Describe the morphology of the erythrocytes.
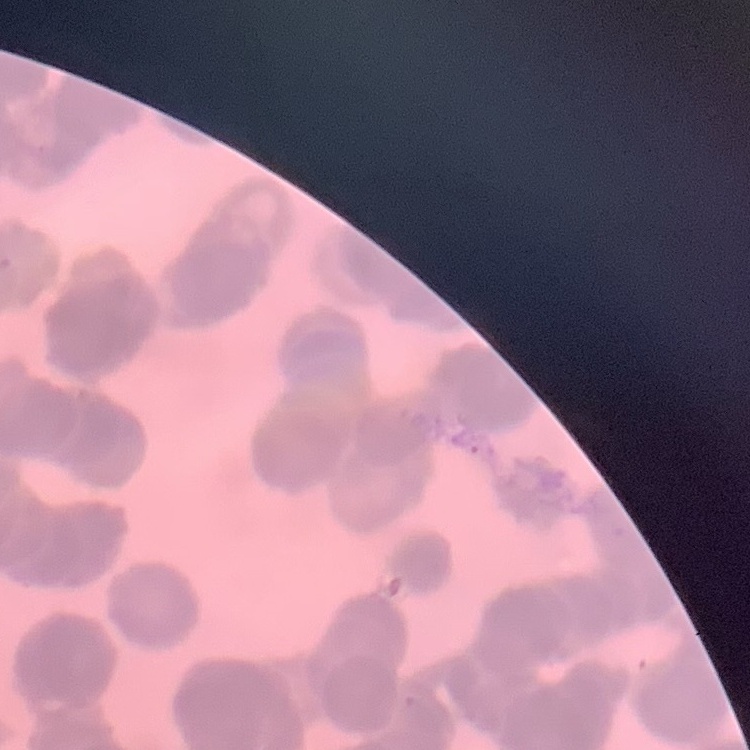

They show rouleaux formation.

preparation = thin blood film
image type = one tile cut from a larger photomicrograph
stain = Field's or Giemsa